Assess this cell for malaria.
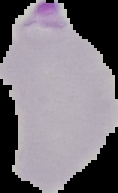

Parasitized.

{
  "image_size": "118×193 pixels",
  "preparation": "thin blood film",
  "image_type": "segmented cell region with the area outside set to black"
}